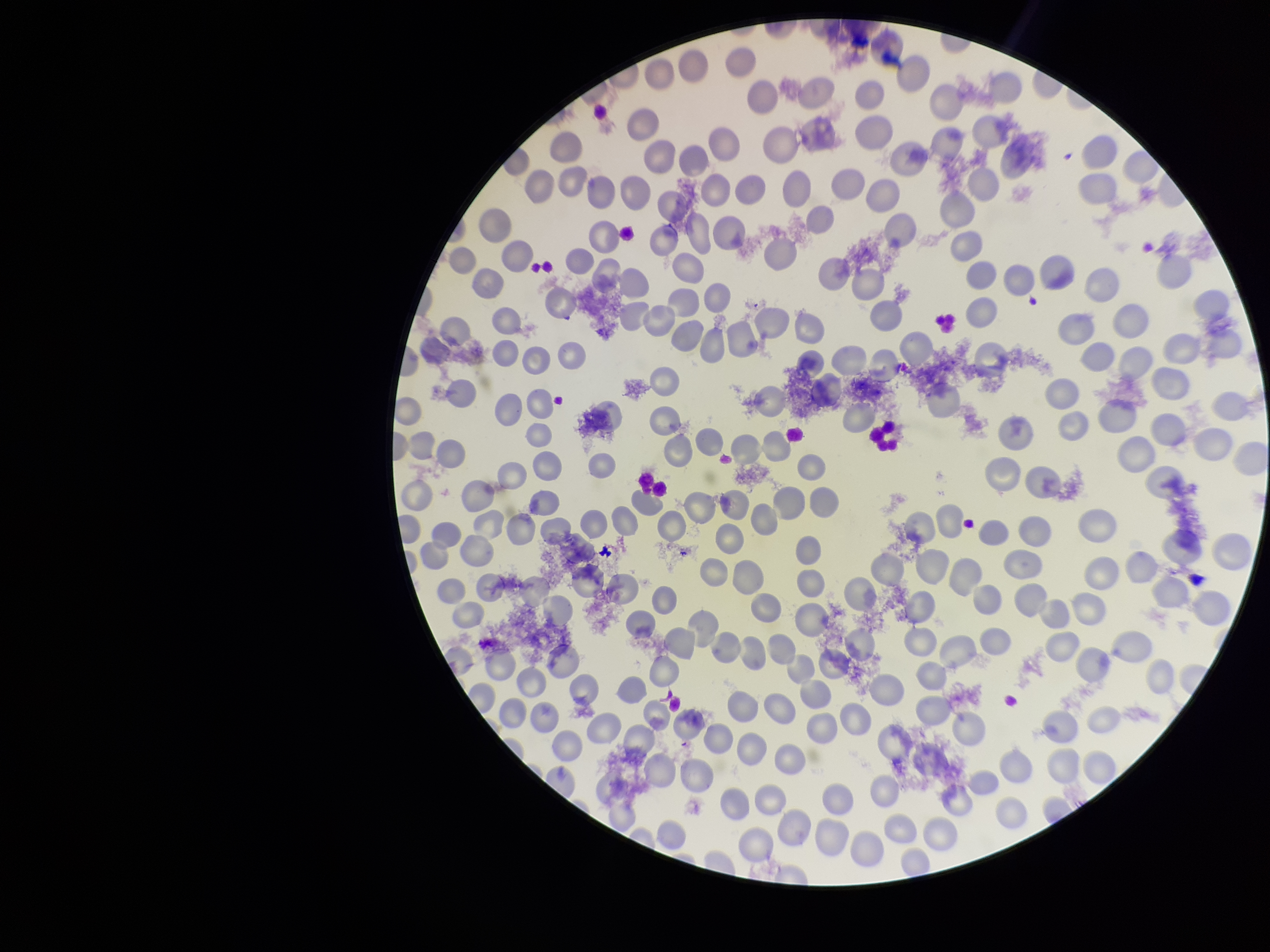

Red blood cell count: 249. Patient malaria status: infected. Parasitized red blood cell count: 0. Smartphone photograph taken through the eyepiece of a microscope. Giemsa stain. Species reported for this patient: Plasmodium falciparum. Preparation: thin. Single field of view. Image is 1270×952 pixels. Parasitized red blood cells: none seen.